Give the extent of all Plasmodium falciparum-infected red blood cells.
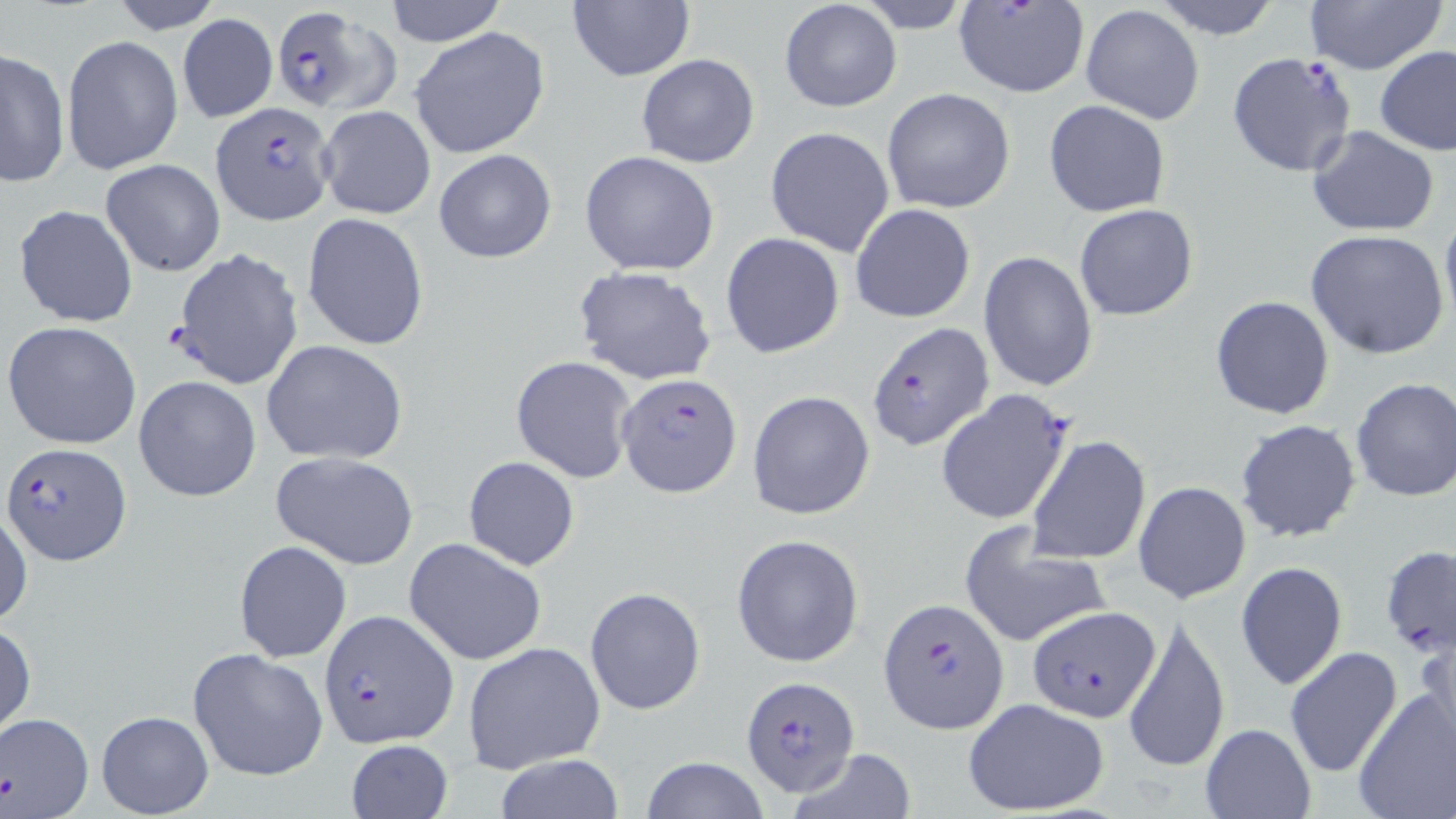

Approximate bounding boxes as (x1,y1)-(x2,y2) corner pairs in pixels.
Plasmodium falciparum-infected red blood cells: (266,3)-(397,114), (1225,53)-(1357,178), (213,102)-(334,225), (867,322)-(994,451), (617,371)-(743,499), (934,388)-(1075,526), (4,442)-(130,566), (876,597)-(1008,733), (1028,604)-(1161,724), (319,610)-(458,746), (738,673)-(861,799).

slide-level diagnosis = Plasmodium falciparum
field of view = single
image size = 1456×819 pixels
stain = May-Grünwald-Giemsa
preparation = thin blood film
magnification = 1000x
modality = optical microscopy
uninfected red blood cell locations = approximate bounding boxes as (x1,y1)-(x2,y2) corner pairs in pixels: (105,0)-(225,34), (382,0)-(507,48), (855,0)-(976,33), (1150,0)-(1284,40), (1301,0)-(1447,76), (778,1)-(903,114), (952,1)-(1090,99), (566,2)-(694,82), (1080,4)-(1206,125), (177,14)-(277,123), (410,27)-(549,159), (60,35)-(181,177), (1375,45)-(1456,157), (1,48)-(71,186), (636,53)-(760,168), (881,87)-(1015,214), (1044,99)-(1170,217), (316,104)-(436,220), (1307,124)-(1440,237), (765,127)-(896,257), (433,149)-(557,264), (579,151)-(720,276), (101,159)-(225,276), (849,202)-(976,323), (13,203)-(139,328), (1074,204)-(1200,321), (1440,204)-(1456,328), (302,212)-(429,351), (1305,229)-(1451,361), (720,231)-(846,360), (171,249)-(304,390), (978,250)-(1099,392), (572,266)-(718,386), (1210,295)-(1335,420), (3,320)-(142,450), (260,339)-(408,464), (511,356)-(635,484), (132,375)-(261,503), (1349,378)-(1456,503), (747,390)-(876,521), (1234,418)-(1363,544), (1026,434)-(1152,566), (271,454)-(418,570), (463,456)-(579,570), (1134,481)-(1252,603), (0,505)-(32,632), (958,525)-(1110,650), (731,533)-(864,669), (403,537)-(549,665), (234,540)-(351,662), (1379,545)-(1456,660), (1235,562)-(1348,690), (585,587)-(706,713), (1123,610)-(1231,776), (1415,618)-(1456,746), (0,622)-(36,739), (462,640)-(608,775), (1282,646)-(1403,778), (188,647)-(329,781), (1353,689)-(1456,819), (963,698)-(1111,817), (95,710)-(213,817), (0,712)-(94,819), (1199,723)-(1316,818), (345,739)-(454,819), (787,748)-(918,818), (494,753)-(625,819), (641,757)-(769,818)